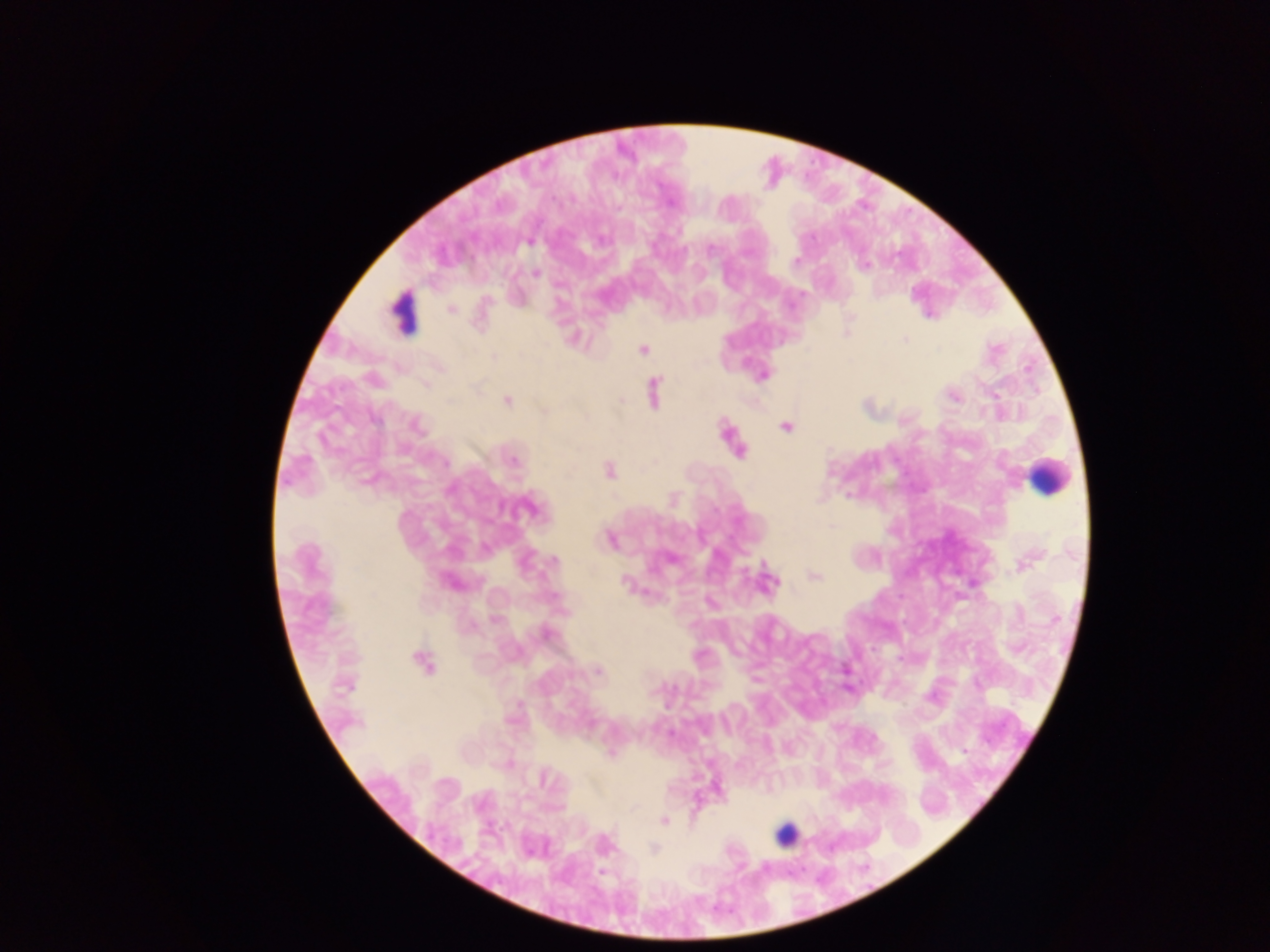 Approximate centers as [x, y] in pixels. Plasmodium parasite locations: [600, 239], [529, 242], [864, 265], [536, 273], [451, 309], [847, 330], [573, 338], [904, 339], [641, 349], [762, 374], [425, 385], [652, 390], [954, 396], [507, 400], [621, 401], [867, 407], [544, 409], [414, 425], [785, 426], [727, 432], [737, 449], [512, 459], [607, 470], [530, 506], [610, 539], [670, 559], [552, 560], [1025, 561], [813, 575], [451, 581], [972, 582], [625, 583], [766, 583], [545, 634], [422, 662], [597, 670], [345, 684], [847, 688], [963, 750], [715, 788], [663, 820], [602, 844], [653, 849]. Leukocyte locations: [402, 311], [1048, 476], [786, 833]. Photographed through a microscope with a mobile-phone camera. Image is 1270×952 pixels. One field of view. Collected in Ghana. Thick blood film.